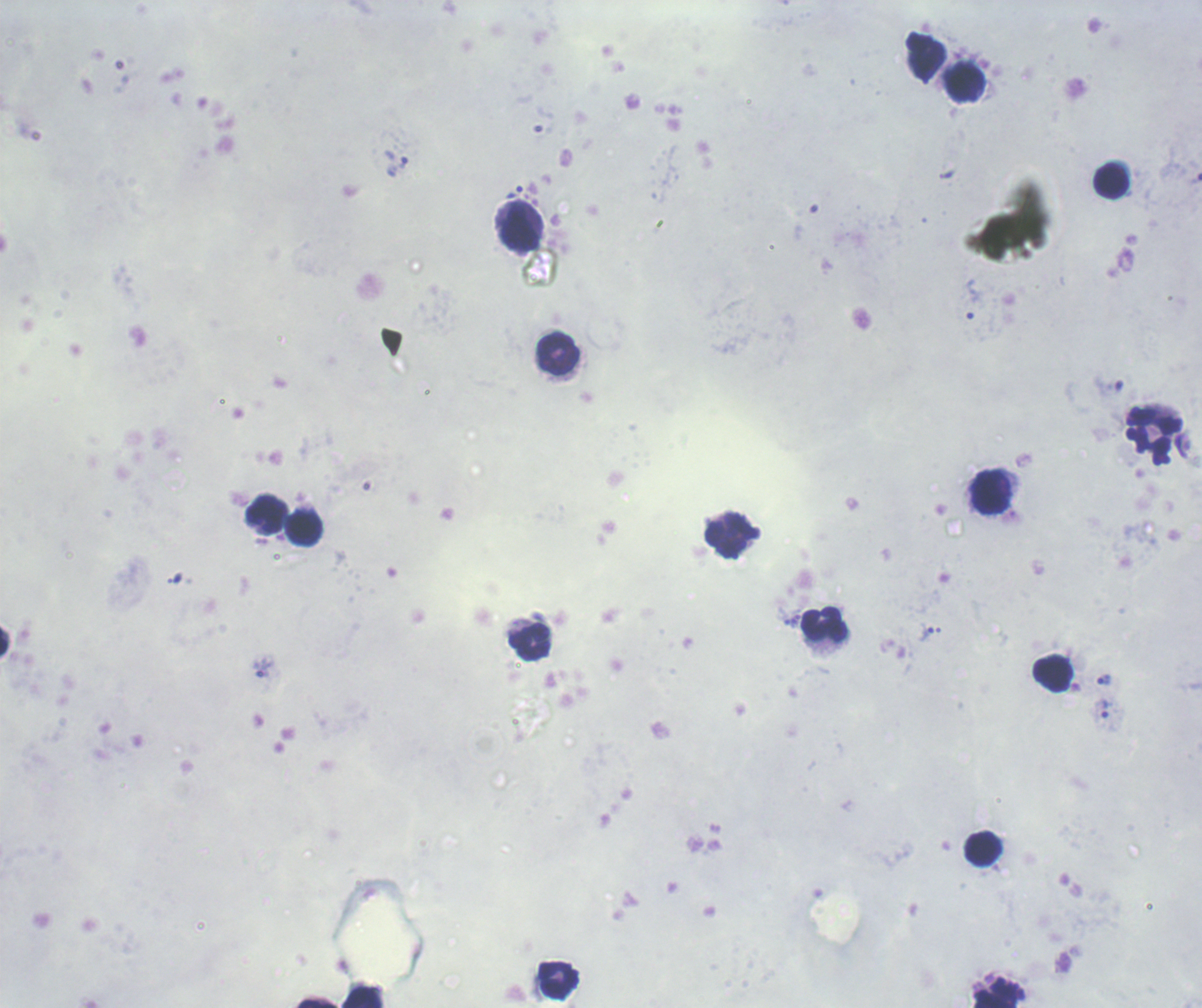
Approximate centers as (x, y) in pixels.
Summary:
  - Trophozoite locations: (947, 175), (515, 191), (1104, 682), (1107, 709)
  - Leukocyte locations: (924, 54), (964, 81), (1110, 181), (521, 226), (555, 351), (1154, 435), (991, 492), (266, 514), (304, 527), (728, 536), (825, 625), (529, 641), (1053, 671), (982, 848), (558, 979), (997, 992), (362, 997), (316, 1003)
  - Preparation: thick blood smear
  - Background quality: poor
  - Result: Plasmodium parasites detected
  - Field of view: one from this slide
  - Image size: 1202×1008 pixels
  - Context: previously used in a real diagnosis
  - Magnification: 100x
  - Stain: Romanowsky